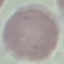

Summary:
  - Result: negative for malaria parasites
  - Preparation: thin blood smear
  - Capture: smartphone camera at the microscope eyepiece
  - Image type: cell patch, automatically extracted from a larger field of view and resized to 64 × 64 pixels
  - Stain: Giemsa